Give the position of every Plasmodium parasite.
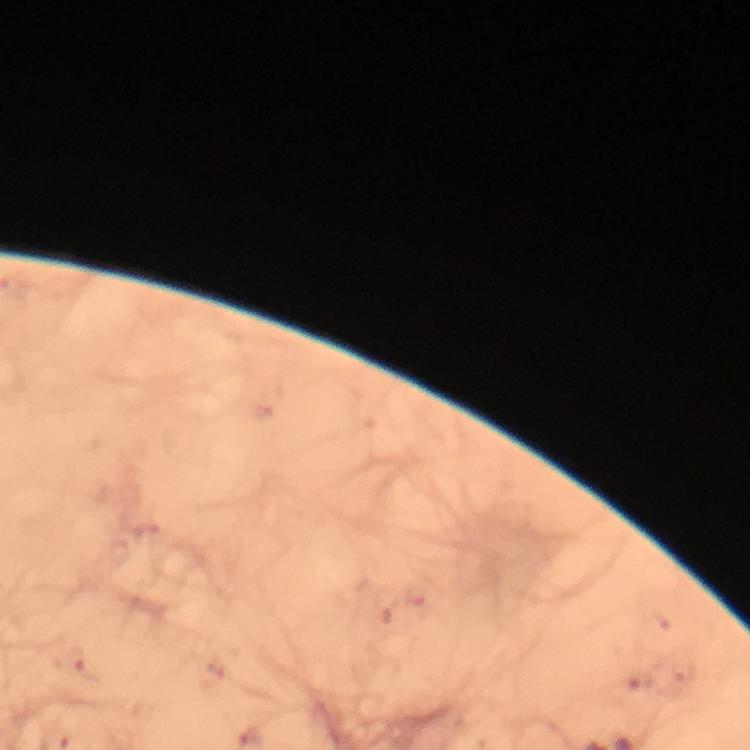

Approximate centers as (x, y) in pixels.
Plasmodium parasites: (145, 533), (418, 597), (73, 663), (214, 666), (684, 672), (636, 680).

{
  "image_size": "750×750 pixels",
  "preparation": "thick blood film",
  "cropped_from": "a single field of view",
  "capture": "smartphone photograph through a microscope",
  "stain": "Giemsa",
  "context": "from a malaria diagnostic workup",
  "immersion_oil": "applied",
  "magnification": "100x"
}